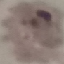
malaria status = parasitized
image type = cell patch, automatically extracted from a larger field of view and resized to 64 × 64 pixels
capture = smartphone camera at the microscope eyepiece
stain = Giemsa
preparation = thin blood smear